Report the malaria status of this cell.
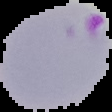

It is parasitized.

image size = 112×112 pixels
preparation = thin blood smear
image type = segmented cell region on a black background